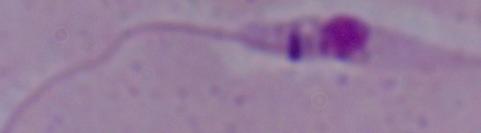
1000x magnification. Micrograph. A Leishmania parasite is seen.